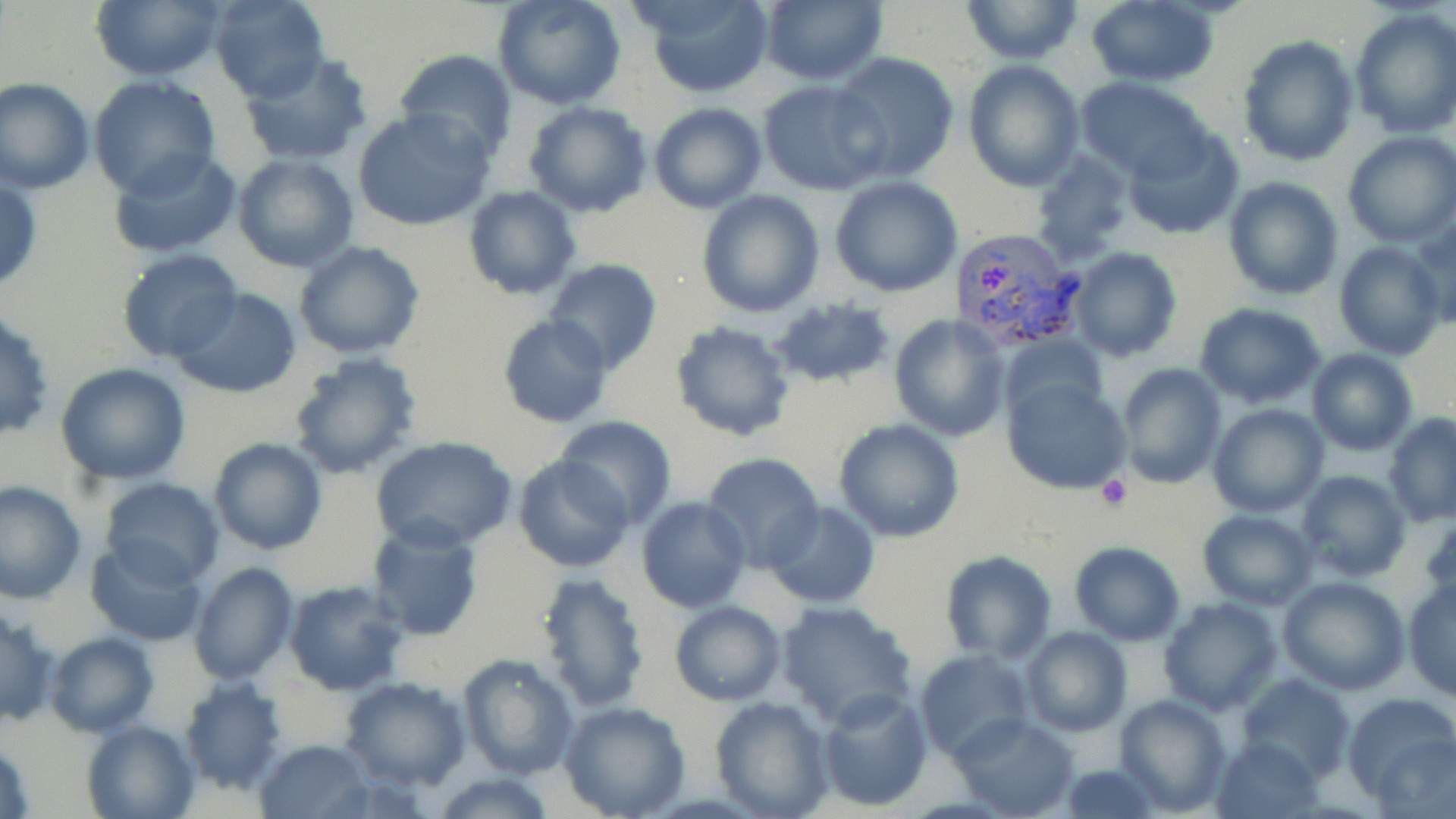

Summary:
  - Coordinate format: approximate bounding boxes as (x1,y1)-(x2,y2) corner pairs in pixels
  - Platelet locations: (1098,475)-(1133,510)
  - Uninfected red blood cell locations: (90,0)-(225,81), (211,0)-(329,102), (634,0)-(776,96), (960,0)-(1083,64), (495,1)-(625,110), (756,1)-(889,86), (1084,2)-(1220,88), (1349,6)-(1456,139), (1238,35)-(1360,168), (395,48)-(516,158), (831,52)-(960,184), (240,53)-(371,165), (963,60)-(1085,191), (0,77)-(93,194), (88,77)-(221,200), (1076,77)-(1213,182), (758,80)-(887,196), (522,101)-(653,219), (648,101)-(768,213), (352,107)-(495,230), (1122,126)-(1246,240), (1342,130)-(1456,247), (107,148)-(242,259), (1028,149)-(1133,264), (232,154)-(359,274), (0,174)-(43,296), (1224,176)-(1342,301), (830,178)-(963,296), (463,186)-(580,298), (695,188)-(825,319), (1414,212)-(1456,333), (293,239)-(425,360), (1334,241)-(1446,361), (1067,247)-(1183,363), (116,250)-(243,364), (546,258)-(662,375), (170,287)-(304,398), (769,297)-(895,387), (1194,303)-(1327,409), (496,314)-(615,429), (887,314)-(1011,441), (671,323)-(795,441), (1000,333)-(1107,427), (1305,348)-(1418,456), (289,353)-(422,479), (56,362)-(190,485), (1114,362)-(1227,488), (1002,376)-(1131,494), (1207,403)-(1328,518), (1385,414)-(1456,525), (554,417)-(677,526), (832,418)-(964,542), (370,436)-(517,552), (208,438)-(327,553), (701,454)-(824,571), (513,455)-(634,573), (1296,469)-(1411,582), (100,478)-(224,587), (1,481)-(87,603), (636,496)-(751,613), (767,500)-(879,608), (1196,509)-(1318,611), (368,521)-(485,640), (84,540)-(206,645), (1066,541)-(1187,645), (940,550)-(1056,663), (190,562)-(298,685), (535,570)-(652,711), (1279,575)-(1409,694), (1404,576)-(1456,701), (284,580)-(408,694), (1159,598)-(1281,715), (776,599)-(920,729), (669,600)-(785,705), (0,608)-(59,731), (1022,625)-(1132,737), (46,632)-(158,737), (914,648)-(1032,762), (458,654)-(579,780), (1237,673)-(1353,783), (339,675)-(472,791), (179,676)-(290,795), (816,685)-(932,809), (1341,692)-(1456,806), (1114,694)-(1231,816), (709,695)-(834,819), (558,701)-(691,819), (950,712)-(1079,819), (81,721)-(197,818), (0,735)-(34,819), (1212,735)-(1326,816), (254,737)-(373,817), (1055,762)-(1164,819), (431,773)-(558,817)
  - Plasmodium vivax-infected red blood cell locations: (946,229)-(1087,352)
  - Slide-level diagnosis: Plasmodium vivax
  - Magnification: 1000x
  - Image size: 1456×819 pixels
  - Stain: May-Grünwald-Giemsa
  - Preparation: thin blood smear
  - Field of view: one of a larger specimen
  - Modality: optical microscopy